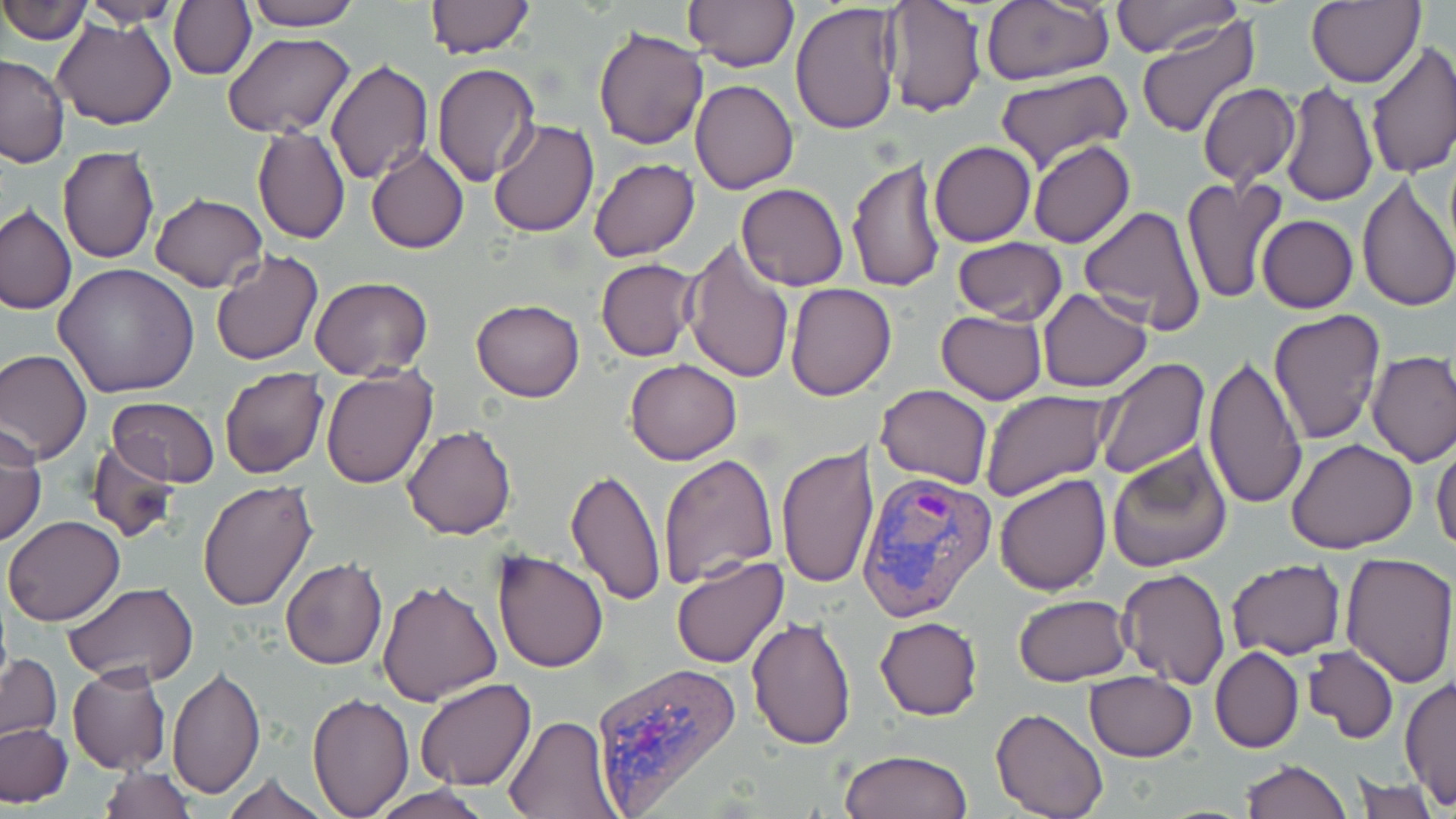

Summary:
  - Coordinate format: approximate bounding boxes as named x1/y1/x2/y2 corners in pixels
  - Plasmodium vivax-infected red blood cell locations: (x1=856, y1=468, x2=997, y2=624), (x1=589, y1=660, x2=742, y2=812)
  - Uninfected red blood cell locations: (x1=0, y1=0, x2=92, y2=47), (x1=81, y1=0, x2=181, y2=27), (x1=239, y1=0, x2=363, y2=31), (x1=682, y1=0, x2=798, y2=71), (x1=982, y1=0, x2=1112, y2=85), (x1=1110, y1=0, x2=1241, y2=57), (x1=170, y1=1, x2=255, y2=80), (x1=424, y1=1, x2=534, y2=59), (x1=882, y1=1, x2=987, y2=117), (x1=1305, y1=2, x2=1425, y2=88), (x1=789, y1=3, x2=905, y2=135), (x1=1135, y1=16, x2=1259, y2=139), (x1=54, y1=18, x2=177, y2=130), (x1=592, y1=26, x2=707, y2=149), (x1=223, y1=32, x2=353, y2=138), (x1=1366, y1=41, x2=1456, y2=180), (x1=0, y1=54, x2=70, y2=166), (x1=324, y1=60, x2=433, y2=184), (x1=432, y1=63, x2=540, y2=186), (x1=992, y1=70, x2=1137, y2=175), (x1=689, y1=79, x2=799, y2=195), (x1=1279, y1=82, x2=1378, y2=207), (x1=1196, y1=83, x2=1300, y2=187), (x1=487, y1=119, x2=598, y2=237), (x1=252, y1=125, x2=350, y2=245), (x1=929, y1=141, x2=1035, y2=247), (x1=1029, y1=141, x2=1135, y2=250), (x1=365, y1=144, x2=470, y2=253), (x1=57, y1=145, x2=160, y2=264), (x1=1045, y1=152, x2=1175, y2=287), (x1=847, y1=156, x2=947, y2=294), (x1=589, y1=157, x2=699, y2=262), (x1=1357, y1=175, x2=1456, y2=314), (x1=1182, y1=177, x2=1285, y2=306), (x1=736, y1=183, x2=849, y2=291), (x1=150, y1=192, x2=267, y2=292), (x1=0, y1=204, x2=76, y2=314), (x1=1078, y1=205, x2=1207, y2=332), (x1=1257, y1=215, x2=1358, y2=312), (x1=952, y1=237, x2=1068, y2=325), (x1=683, y1=240, x2=795, y2=384), (x1=209, y1=248, x2=324, y2=367), (x1=595, y1=258, x2=700, y2=361), (x1=53, y1=263, x2=200, y2=397), (x1=310, y1=276, x2=433, y2=379), (x1=786, y1=282, x2=896, y2=400), (x1=1037, y1=288, x2=1152, y2=392), (x1=471, y1=299, x2=585, y2=401), (x1=1269, y1=309, x2=1387, y2=443), (x1=935, y1=310, x2=1046, y2=405), (x1=0, y1=347, x2=91, y2=464), (x1=1366, y1=350, x2=1456, y2=466), (x1=1092, y1=356, x2=1211, y2=478), (x1=1201, y1=356, x2=1308, y2=511), (x1=626, y1=359, x2=741, y2=464), (x1=321, y1=367, x2=438, y2=488), (x1=219, y1=368, x2=329, y2=479), (x1=876, y1=383, x2=993, y2=490), (x1=981, y1=390, x2=1113, y2=501), (x1=106, y1=397, x2=220, y2=487), (x1=1, y1=420, x2=46, y2=547), (x1=403, y1=426, x2=516, y2=540), (x1=1432, y1=436, x2=1456, y2=558), (x1=1287, y1=438, x2=1419, y2=554), (x1=87, y1=440, x2=182, y2=543), (x1=1106, y1=441, x2=1233, y2=573), (x1=776, y1=443, x2=879, y2=591), (x1=658, y1=453, x2=782, y2=587), (x1=565, y1=468, x2=666, y2=606), (x1=992, y1=471, x2=1111, y2=595), (x1=198, y1=478, x2=318, y2=612), (x1=2, y1=513, x2=126, y2=626), (x1=493, y1=551, x2=608, y2=673), (x1=1338, y1=552, x2=1455, y2=688), (x1=671, y1=555, x2=788, y2=668), (x1=1225, y1=559, x2=1345, y2=658), (x1=280, y1=560, x2=387, y2=670), (x1=1117, y1=567, x2=1231, y2=689), (x1=377, y1=578, x2=503, y2=705), (x1=63, y1=582, x2=199, y2=686), (x1=1013, y1=595, x2=1131, y2=686), (x1=746, y1=616, x2=857, y2=751), (x1=875, y1=616, x2=982, y2=719), (x1=1303, y1=646, x2=1399, y2=744), (x1=1211, y1=647, x2=1304, y2=753), (x1=1, y1=655, x2=62, y2=743), (x1=67, y1=663, x2=171, y2=774), (x1=167, y1=668, x2=265, y2=801), (x1=1084, y1=671, x2=1197, y2=760), (x1=414, y1=677, x2=535, y2=793), (x1=1400, y1=677, x2=1455, y2=809), (x1=307, y1=692, x2=413, y2=815), (x1=992, y1=707, x2=1109, y2=819), (x1=503, y1=714, x2=621, y2=818), (x1=1, y1=722, x2=73, y2=807), (x1=838, y1=750, x2=972, y2=819), (x1=1241, y1=760, x2=1350, y2=819), (x1=100, y1=764, x2=194, y2=819), (x1=220, y1=773, x2=332, y2=818), (x1=1354, y1=775, x2=1440, y2=819), (x1=369, y1=786, x2=494, y2=819)
  - Slide-level diagnosis: Plasmodium vivax
  - Magnification: 1000x
  - Stain: May-Grünwald-Giemsa
  - Preparation: thin blood film
  - Image size: 1456×819 pixels
  - Field of view: single
  - Modality: optical microscopy